Assess this cell for malaria.
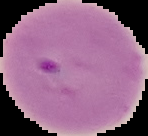

It is parasitized.

Summary:
  - Preparation: thin blood smear
  - Image size: 148×136 pixels
  - Image type: segmented cell region with the area outside set to black